Classify this cell by malaria status.
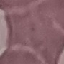

It is uninfected.

preparation = thin blood film
capture = smartphone through the microscope eyepiece
image type = automatically extracted cell patch, resized to 64 × 64 pixels
stain = Giemsa